Identify the blood parasite species.
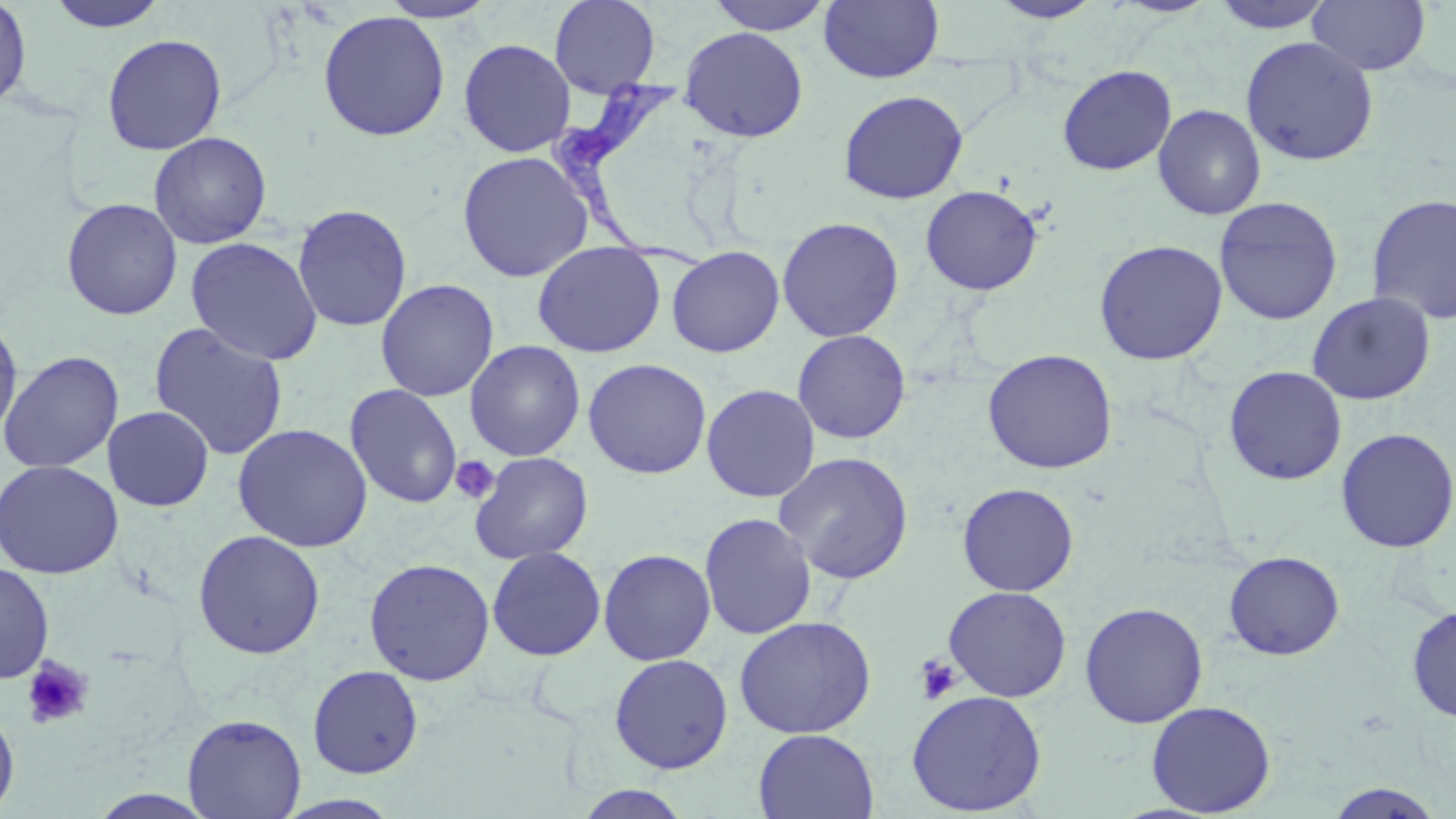
Trypanosoma brucei.

Summary:
  - Coordinate format: approximate bounding boxes as named x1/y1/x2/y2 corners in pixels
  - Trypanosoma brucei locations: (x1=547, y1=70, x2=711, y2=276)
  - Platelet locations: (x1=450, y1=456, x2=499, y2=504), (x1=913, y1=653, x2=964, y2=704), (x1=22, y1=655, x2=94, y2=729)
  - Uninfected red blood cell locations: (x1=0, y1=0, x2=33, y2=112), (x1=379, y1=0, x2=499, y2=23), (x1=549, y1=0, x2=661, y2=97), (x1=703, y1=0, x2=835, y2=35), (x1=819, y1=0, x2=944, y2=84), (x1=1210, y1=0, x2=1336, y2=33), (x1=1307, y1=0, x2=1430, y2=77), (x1=45, y1=1, x2=171, y2=33), (x1=987, y1=1, x2=1104, y2=23), (x1=1278, y1=9, x2=1415, y2=119), (x1=317, y1=10, x2=451, y2=141), (x1=679, y1=26, x2=808, y2=142), (x1=101, y1=33, x2=227, y2=155), (x1=1240, y1=36, x2=1379, y2=166), (x1=458, y1=38, x2=576, y2=158), (x1=1057, y1=64, x2=1177, y2=176), (x1=838, y1=89, x2=968, y2=204), (x1=1153, y1=104, x2=1267, y2=220), (x1=148, y1=131, x2=272, y2=250), (x1=456, y1=150, x2=594, y2=283), (x1=920, y1=185, x2=1042, y2=296), (x1=1366, y1=194, x2=1456, y2=325), (x1=1214, y1=196, x2=1343, y2=326), (x1=60, y1=197, x2=183, y2=321), (x1=292, y1=203, x2=413, y2=332), (x1=777, y1=217, x2=904, y2=342), (x1=185, y1=236, x2=323, y2=366), (x1=1093, y1=239, x2=1228, y2=365), (x1=532, y1=241, x2=666, y2=358), (x1=666, y1=245, x2=785, y2=358), (x1=375, y1=278, x2=499, y2=402), (x1=1307, y1=291, x2=1436, y2=406), (x1=0, y1=318, x2=23, y2=442), (x1=148, y1=322, x2=290, y2=460), (x1=792, y1=329, x2=911, y2=444), (x1=464, y1=339, x2=585, y2=462), (x1=982, y1=348, x2=1118, y2=474), (x1=0, y1=350, x2=124, y2=474), (x1=582, y1=358, x2=712, y2=479), (x1=1224, y1=365, x2=1347, y2=486), (x1=345, y1=383, x2=463, y2=509), (x1=700, y1=384, x2=820, y2=502), (x1=103, y1=406, x2=215, y2=512), (x1=232, y1=422, x2=374, y2=553), (x1=1336, y1=427, x2=1456, y2=553), (x1=773, y1=451, x2=915, y2=584), (x1=469, y1=452, x2=594, y2=564), (x1=0, y1=459, x2=123, y2=580), (x1=957, y1=483, x2=1079, y2=596), (x1=699, y1=512, x2=817, y2=640), (x1=191, y1=529, x2=326, y2=660), (x1=486, y1=546, x2=607, y2=662), (x1=598, y1=548, x2=717, y2=665), (x1=1223, y1=551, x2=1345, y2=660), (x1=363, y1=557, x2=495, y2=686), (x1=0, y1=561, x2=55, y2=684), (x1=943, y1=586, x2=1072, y2=702), (x1=1079, y1=602, x2=1208, y2=728), (x1=1406, y1=605, x2=1456, y2=723), (x1=734, y1=615, x2=876, y2=739), (x1=608, y1=653, x2=733, y2=774), (x1=307, y1=664, x2=423, y2=778), (x1=906, y1=689, x2=1047, y2=816), (x1=1146, y1=700, x2=1276, y2=816), (x1=0, y1=706, x2=19, y2=815), (x1=182, y1=713, x2=306, y2=819), (x1=752, y1=729, x2=879, y2=818), (x1=1323, y1=782, x2=1448, y2=818), (x1=572, y1=785, x2=695, y2=819), (x1=273, y1=794, x2=405, y2=819)
  - Magnification: 1000x
  - Stain: May-Grünwald-Giemsa
  - Modality: light microscopy
  - Field of view: one of a larger specimen
  - Preparation: thin blood smear
  - Image size: 1456×819 pixels